Report the malaria status of this cell.
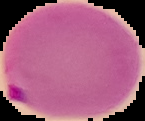

It is parasitized.

Image is 145×121 pixels. Segmented cell region on a black background. From a thin blood film.